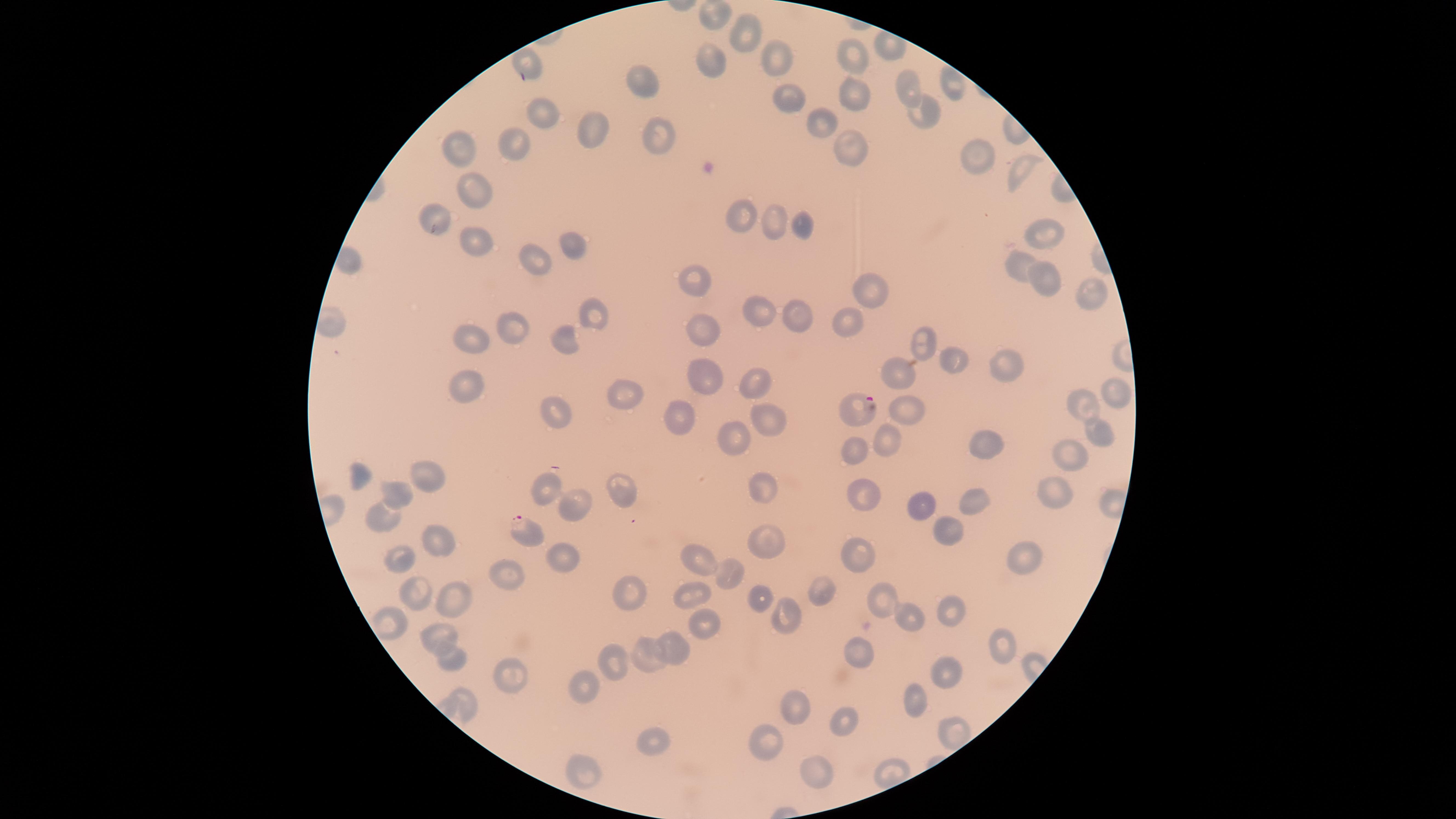 Approximate marker points as {x, y} in pixels. Parasitized red blood cells: {858, 406}, {523, 531}. Uninfected red blood cells: {713, 14}, {741, 34}, {526, 56}, {779, 56}, {846, 56}, {711, 59}, {642, 78}, {953, 82}, {905, 85}, {846, 91}, {783, 102}, {539, 112}, {920, 114}, {822, 120}, {595, 129}, {655, 137}, {517, 138}, {464, 144}, {849, 146}, {974, 154}, {1021, 171}, {476, 186}, {435, 215}, {742, 217}, {777, 223}, {802, 226}, {1047, 233}, {464, 236}, {571, 242}, {531, 256}, {1016, 259}, {1038, 275}, {697, 279}, {871, 288}, {1087, 291}, {801, 312}, {596, 313}, {760, 313}, {845, 318}, {706, 325}, {512, 329}, {471, 336}, {564, 338}, {924, 341}, {952, 359}, {1006, 362}, {703, 375}, {896, 376}, {747, 380}, {1111, 381}, {470, 385}, {621, 389}, {1081, 401}, {912, 406}, {548, 410}, {682, 414}, {762, 417}, {1097, 428}, {734, 435}, {888, 441}, {852, 442}, {985, 442}, {1068, 456}, {429, 469}, {355, 474}, {541, 485}, {616, 485}, {760, 485}, {864, 492}, {1056, 492}, {393, 495}, {973, 497}, {571, 506}, {927, 509}, {385, 516}, {948, 528}, {761, 537}, {435, 540}, {1026, 552}, {553, 553}, {858, 554}, {402, 557}, {699, 560}, {728, 574}, {505, 577}, {817, 586}, {758, 589}, {628, 596}, {416, 597}, {453, 597}, {692, 597}, {887, 601}, {949, 604}, {790, 614}, {914, 617}, {699, 626}, {437, 635}, {1006, 638}, {675, 649}, {649, 651}, {859, 656}, {620, 658}, {457, 660}, {947, 668}, {512, 669}, {586, 683}, {463, 700}, {919, 703}, {800, 706}, {842, 718}, {758, 740}, {651, 741}, {817, 770}, {580, 773}. Image is 1456×819 pixels. Circular visible region. Giemsa-stained preparation. Thin smear of blood. Photographed with a smartphone camera through the microscope eyepiece. Presence: malaria parasites identified. Species: Plasmodium falciparum. One field of view of the specimen.